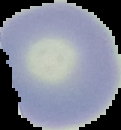

Summary:
  - Preparation: thin blood smear
  - Malaria status: uninfected
  - Image type: cell region segmented out of the field of view; surrounding area masked to black
  - Image size: 121×130 pixels